Report the malaria status of this cell.
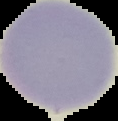

It is uninfected.

image type = segmented cell region on a black background
image size = 118×121 pixels
preparation = thin blood film